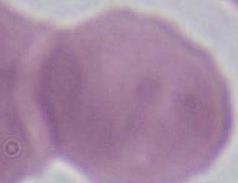

Summary:
  - Identification: erythrocyte
  - Magnification: 1000x
  - Modality: photomicrograph